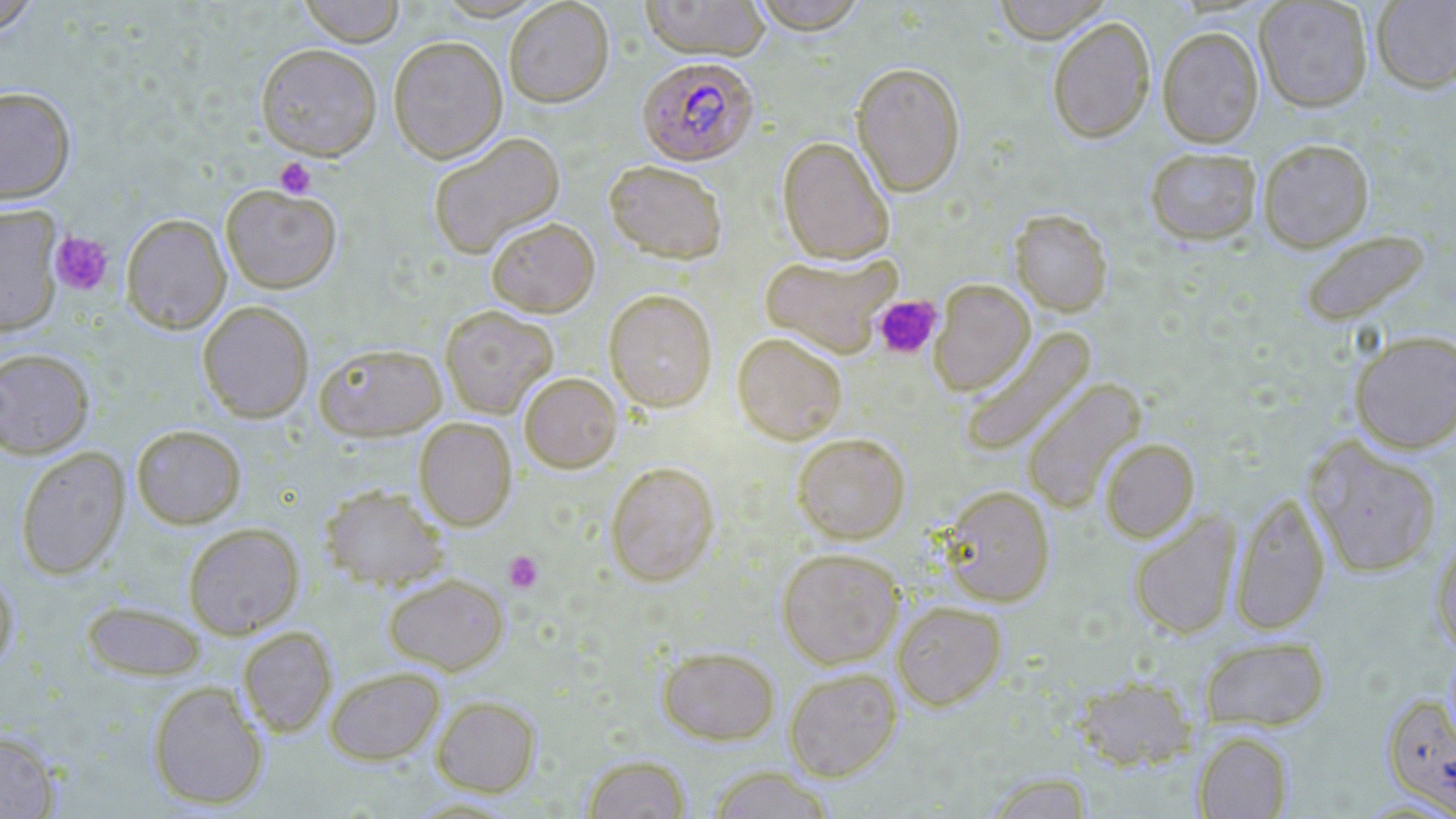 Approximate bounding boxes as (x1,y1)-(x2,y2) corner pairs in pixels. Uninfected red blood cell locations (subset): (0,0)-(41,36), (297,0)-(406,46), (640,0)-(770,60), (749,0)-(869,34), (991,0)-(1114,43), (1371,0)-(1456,93), (504,1)-(614,107), (1254,1)-(1373,112), (1047,16)-(1155,143), (1157,26)-(1264,147), (388,35)-(508,163), (256,43)-(382,159), (851,62)-(966,197), (0,85)-(76,204), (427,131)-(565,258), (777,136)-(895,264), (1257,138)-(1375,252), (1144,146)-(1263,245), (604,160)-(728,263), (221,184)-(341,293), (0,205)-(63,336), (1009,209)-(1113,317), (120,213)-(231,333), (485,217)-(600,317), (1299,229)-(1430,326), (760,252)-(901,357), (929,279)-(1035,396), (604,289)-(717,412), (198,301)-(314,423), (440,305)-(559,418), (959,327)-(1096,458), (1349,330)-(1456,453), (731,331)-(848,444), (314,342)-(446,440), (0,347)-(95,459), (519,372)-(622,473), (1022,378)-(1146,513), (414,417)-(516,530), (131,424)-(247,528), (792,432)-(910,544), (1099,438)-(1199,543), (1304,438)-(1442,578), (15,447)-(130,579), (605,461)-(720,585), (320,485)-(448,591), (939,485)-(1056,606), (1229,491)-(1331,636), (1129,512)-(1240,640), (183,522)-(304,638), (1431,531)-(1456,657), (777,547)-(903,669), (0,565)-(18,674), (382,573)-(509,674), (81,599)-(208,682), (892,600)-(1007,710), (238,626)-(337,737), (1199,636)-(1330,731), (657,646)-(780,744), (325,667)-(444,764), (784,667)-(902,781), (1071,674)-(1198,770), (147,680)-(269,810), (432,695)-(541,796), (0,730)-(60,818), (1193,730)-(1293,818), (582,755)-(693,819), (706,766)-(835,818), (983,772)-(1095,818). Platelet locations: (274,157)-(316,199), (49,230)-(114,296), (872,294)-(943,359), (504,550)-(544,593). Plasmodium falciparum-infected red blood cell locations (subset): (637,56)-(758,165). Slide-level diagnosis: Plasmodium falciparum. Light microscopy. Thin blood film. May-Grünwald-Giemsa stain. Image is 1456×819 pixels. One field of a larger specimen. 1000x magnification.